State which cell type is depicted.
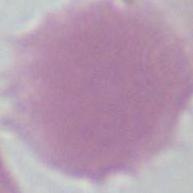
This is an erythrocyte.

{
  "magnification": "1000x",
  "modality": "photomicrograph"
}